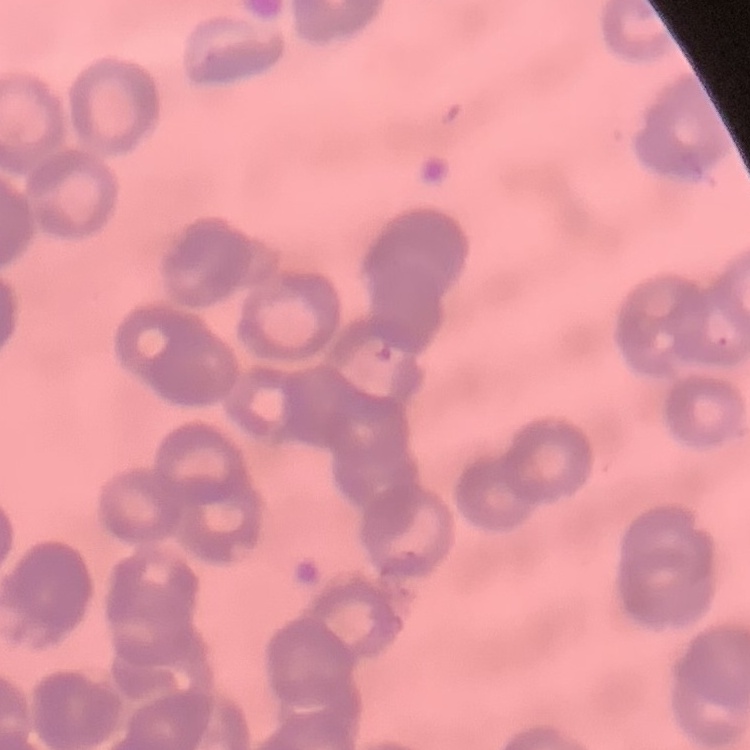
Summary:
  - Erythrocyte morphology: rouleaux formation
  - Image type: one tile cut from a larger photomicrograph
  - Stain: Field's or Giemsa
  - Preparation: thin blood smear